Name the parasite shown.
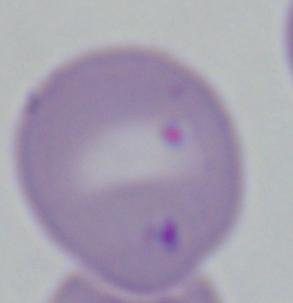
This is Babesia.

1000x magnification. Photomicrograph.